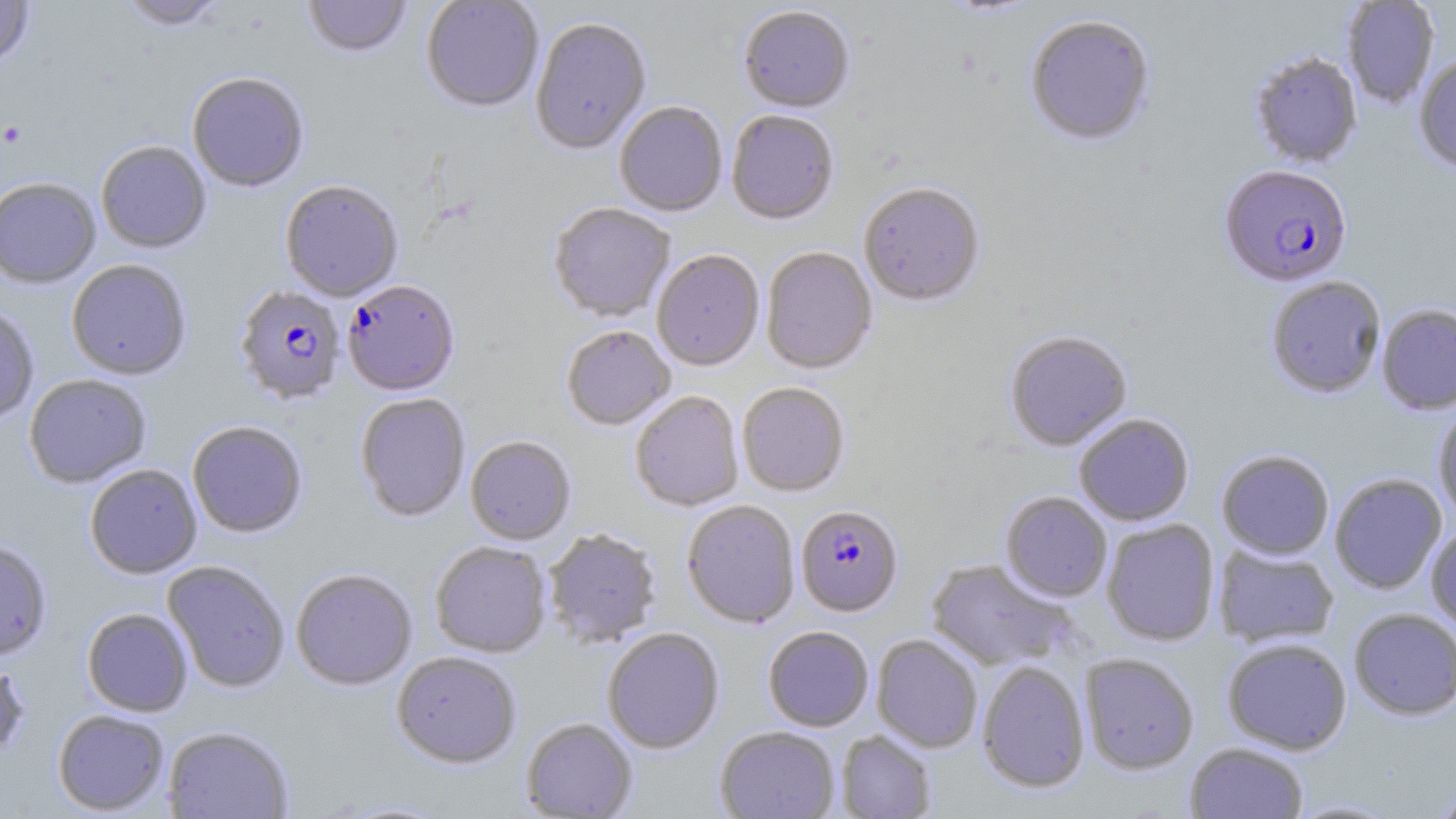
slide_level_diagnosis: Plasmodium falciparum
magnification: 1000x
stain: May-Grünwald-Giemsa
image_size: 1456×819 pixels
modality: optical microscopy
plasmodium_falciparum_infected_red_blood_cell_locations: 'approximate bounding boxes as named x1/y1/x2/y2 corners in pixels: (x1=1219, y1=166, x2=1352, y2=288), (x1=342, y1=281, x2=460, y2=397), (x1=233, y1=286, x2=346, y2=406), (x1=796, y1=505, x2=903, y2=617)'
field_of_view: one of a larger specimen
preparation: thin blood smear
platelet_locations: 'approximate bounding boxes as named x1/y1/x2/y2 corners in pixels: (x1=1, y1=121, x2=28, y2=147)'
uninfected_red_blood_cell_locations: 'approximate bounding boxes as named x1/y1/x2/y2 corners in pixels: (x1=0, y1=0, x2=35, y2=70), (x1=118, y1=0, x2=226, y2=33), (x1=303, y1=0, x2=412, y2=60), (x1=421, y1=0, x2=544, y2=115), (x1=939, y1=0, x2=1045, y2=19), (x1=1342, y1=0, x2=1440, y2=108), (x1=738, y1=8, x2=854, y2=115), (x1=1026, y1=16, x2=1155, y2=147), (x1=531, y1=19, x2=651, y2=157), (x1=1248, y1=53, x2=1363, y2=169), (x1=1414, y1=56, x2=1456, y2=175), (x1=187, y1=74, x2=309, y2=193), (x1=614, y1=102, x2=728, y2=217), (x1=726, y1=111, x2=839, y2=226), (x1=95, y1=142, x2=211, y2=254), (x1=0, y1=178, x2=101, y2=289), (x1=280, y1=181, x2=403, y2=303), (x1=858, y1=183, x2=984, y2=308), (x1=548, y1=204, x2=675, y2=323), (x1=760, y1=248, x2=877, y2=376), (x1=651, y1=251, x2=765, y2=372), (x1=66, y1=260, x2=192, y2=380), (x1=1266, y1=277, x2=1386, y2=399), (x1=0, y1=304, x2=39, y2=425), (x1=1377, y1=304, x2=1456, y2=415), (x1=561, y1=326, x2=675, y2=431), (x1=1005, y1=332, x2=1132, y2=452), (x1=24, y1=375, x2=152, y2=489), (x1=737, y1=383, x2=849, y2=497), (x1=630, y1=392, x2=744, y2=512), (x1=355, y1=394, x2=470, y2=523), (x1=1433, y1=405, x2=1456, y2=523), (x1=1074, y1=414, x2=1194, y2=526), (x1=187, y1=422, x2=308, y2=539), (x1=466, y1=437, x2=576, y2=546), (x1=1217, y1=450, x2=1334, y2=560), (x1=85, y1=464, x2=202, y2=579), (x1=1329, y1=473, x2=1447, y2=594), (x1=1000, y1=492, x2=1112, y2=602), (x1=682, y1=501, x2=800, y2=629), (x1=1101, y1=519, x2=1220, y2=646), (x1=1425, y1=524, x2=1456, y2=634), (x1=543, y1=530, x2=661, y2=649), (x1=0, y1=539, x2=52, y2=661), (x1=430, y1=542, x2=551, y2=658), (x1=1212, y1=544, x2=1339, y2=648), (x1=925, y1=559, x2=1075, y2=671), (x1=163, y1=561, x2=290, y2=693), (x1=291, y1=569, x2=417, y2=691), (x1=82, y1=608, x2=193, y2=717), (x1=1348, y1=609, x2=1456, y2=720), (x1=763, y1=626, x2=874, y2=731), (x1=602, y1=629, x2=724, y2=754), (x1=871, y1=635, x2=982, y2=753), (x1=1222, y1=638, x2=1352, y2=755), (x1=392, y1=652, x2=521, y2=769), (x1=1079, y1=654, x2=1199, y2=774), (x1=0, y1=658, x2=29, y2=759), (x1=977, y1=661, x2=1091, y2=794), (x1=53, y1=709, x2=169, y2=816), (x1=520, y1=718, x2=637, y2=818), (x1=163, y1=726, x2=294, y2=819), (x1=715, y1=726, x2=840, y2=819), (x1=836, y1=730, x2=937, y2=819), (x1=1185, y1=743, x2=1308, y2=818), (x1=1430, y1=781, x2=1456, y2=819), (x1=1286, y1=798, x2=1404, y2=818), (x1=329, y1=799, x2=456, y2=818)'